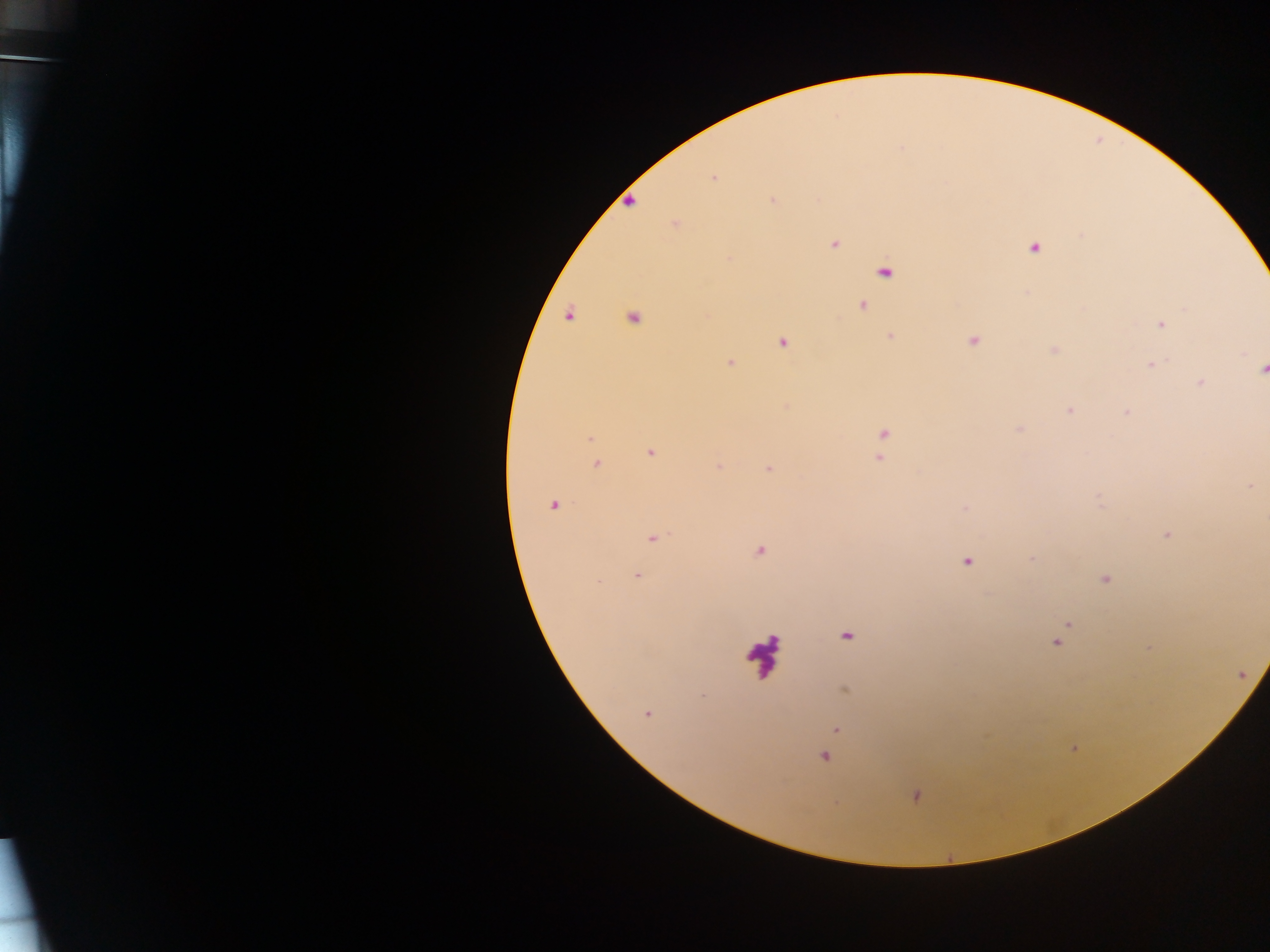

Approximate centers as x y in pixels.
Summary:
  - Leukocyte locations: 761 652
  - Malaria parasite locations (subset; some below the resolvable size): 900 147; 711 178; 772 200; 674 224; 1082 236; 834 244; 1035 247; 730 259; 793 268; 861 305; 1184 308; 632 315; 1161 323; 890 336; 973 340; 783 343; 730 361; 1150 365; 1262 369; 1200 383; 786 406; 1068 409; 1124 412; 883 434; 592 438; 649 452; 880 457; 598 465; 719 466; 769 469; 1249 486; 553 504; 1166 535; 654 537; 759 550; 966 561; 638 576; 1103 579; 599 582; 1068 623; 847 636; 1056 643; 845 690; 703 695; 646 713; 837 729; 825 756; 916 796
  - Country: Ghana
  - Field of view: single
  - Capture: mobile-phone photograph through a microscope
  - Preparation: thick blood film
  - Image size: 1270×952 pixels